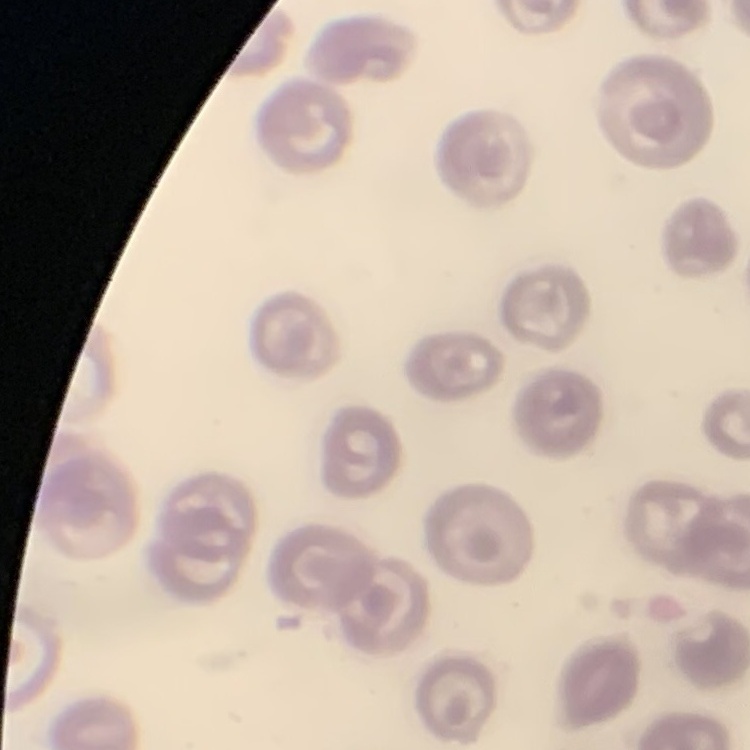
Summary:
  - Erythrocyte morphology: no rouleaux formation
  - Preparation: thin blood film
  - Image type: one tile cut from a larger photomicrograph
  - Stain: Field's or Giemsa